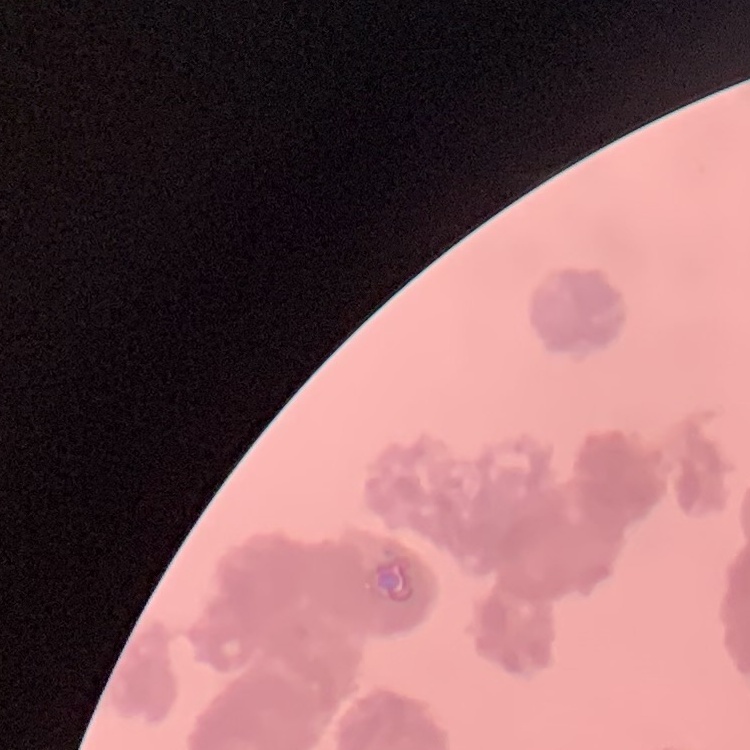

Summary:
  - Red blood cell morphology: rouleaux formation
  - Stain: Field's or Giemsa
  - Image type: one tile cut from a larger photomicrograph
  - Preparation: thin peripheral smear